Name the parasite shown.
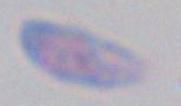

This is Toxoplasma gondii.

Summary:
  - Magnification: 1000x
  - Modality: photomicrograph